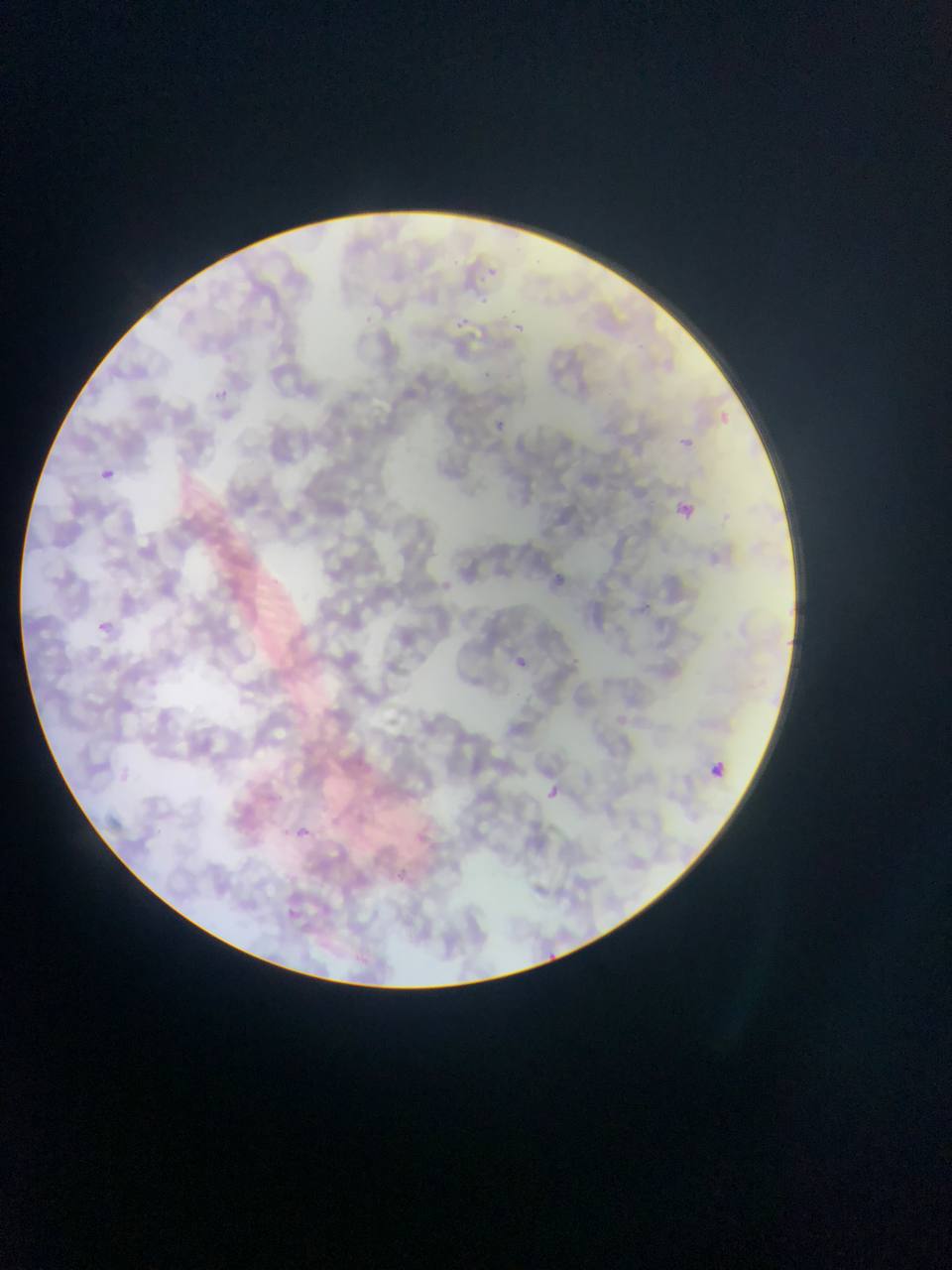
Approximate bounding boxes as {left, top, right, bottom} in pixels. Malaria parasite locations: {478, 258, 503, 279}, {469, 288, 491, 309}, {354, 312, 377, 332}, {511, 314, 536, 331}, {460, 321, 492, 344}, {477, 362, 500, 380}, {213, 385, 249, 409}, {714, 400, 739, 430}, {490, 420, 518, 440}, {682, 430, 699, 453}, {95, 458, 129, 494}, {675, 502, 696, 527}, {554, 567, 573, 592}, {431, 576, 467, 592}, {97, 621, 110, 632}, {511, 645, 538, 678}, {706, 756, 733, 787}, {544, 780, 562, 813}, {284, 818, 312, 839}. Sample from Ghana. Photographed through a microscope with a mobile-phone camera. Image is 952×1270 pixels. One field of view. Thin blood film.